Classify this cell by malaria status.
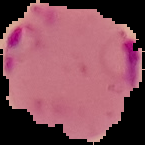
Parasitized.

preparation = thin blood smear
image size = 145×145 pixels
image type = cell region segmented out of the field of view; surrounding area masked to black